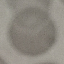

Summary:
  - Result: no malaria parasites detected
  - Stain: Giemsa
  - Image type: cell patch, automatically extracted from a larger field of view and resized to 64 × 64 pixels
  - Capture: smartphone camera at the microscope eyepiece
  - Preparation: thin smear